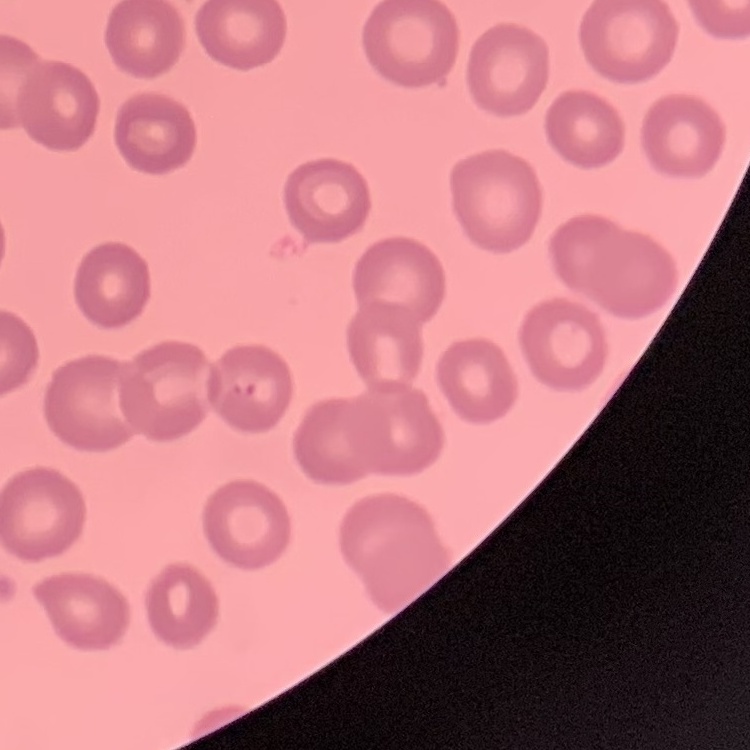
red blood cell morphology = no rouleaux formation
stain = Field's or Giemsa
preparation = thin blood film
image type = square crop of a larger photomicrograph